Assess this cell for malaria.
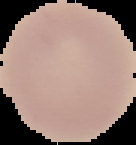
Uninfected.

Cell region segmented out of the field of view; the surrounding area is masked to black. From a thin blood film. Image is 136×145 pixels.